State which cell type is depicted.
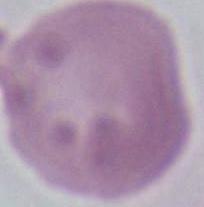

An erythrocyte.

Summary:
  - Magnification: 1000x
  - Modality: micrograph